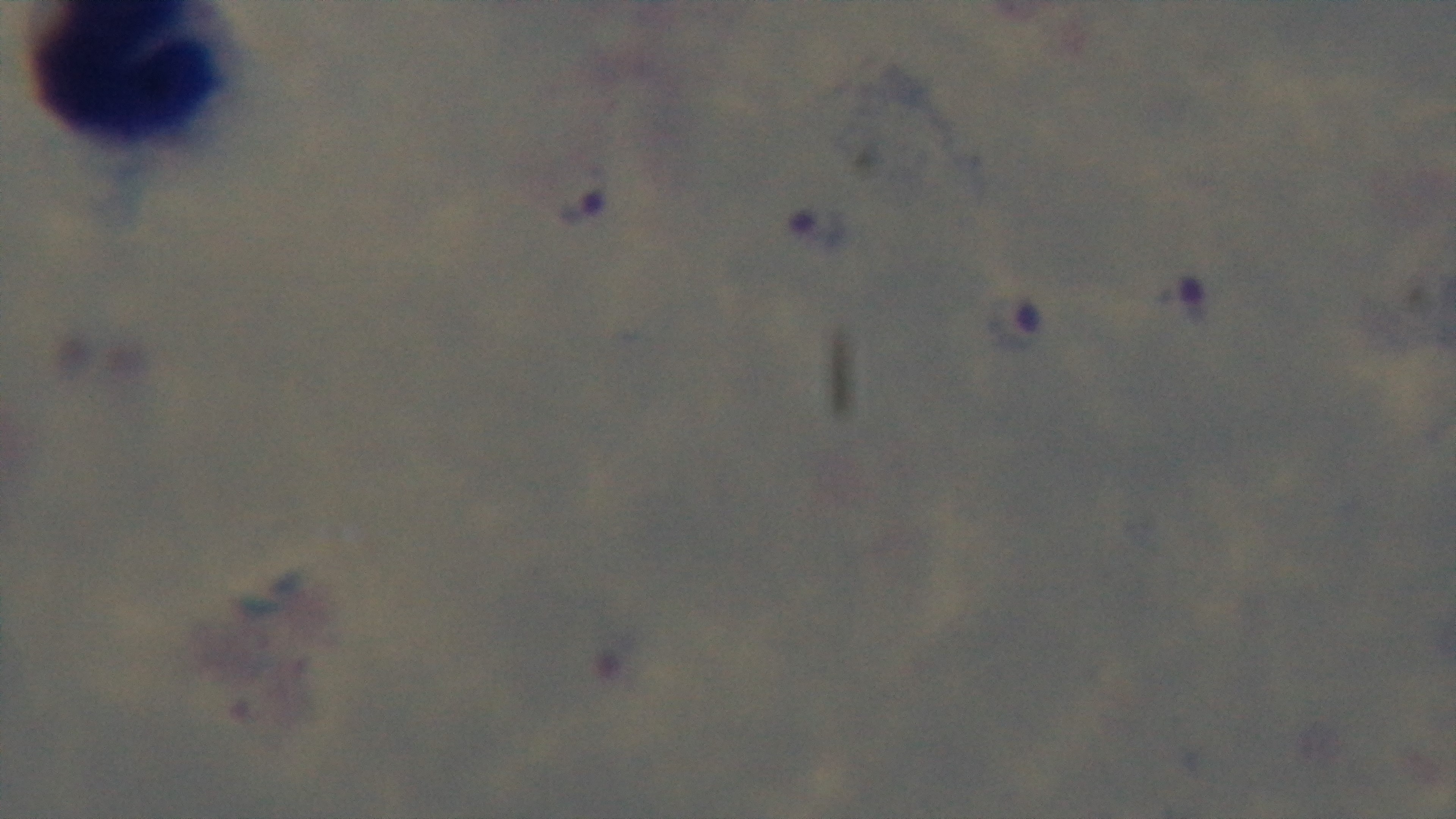 Preparation: thick blood film. Single field of view. Giemsa-stained. Light microscopy. Oil-immersion objective, 100x. Malaria status: positive. Mounted 4K digital camera.